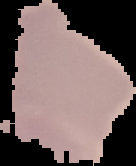
Summary:
  - Preparation: thin blood smear
  - Malaria status: uninfected
  - Image size: 136×166 pixels
  - Image type: segmented cell region with the area outside set to black